Draw a bounding box around every leukocyte (white blood cell).
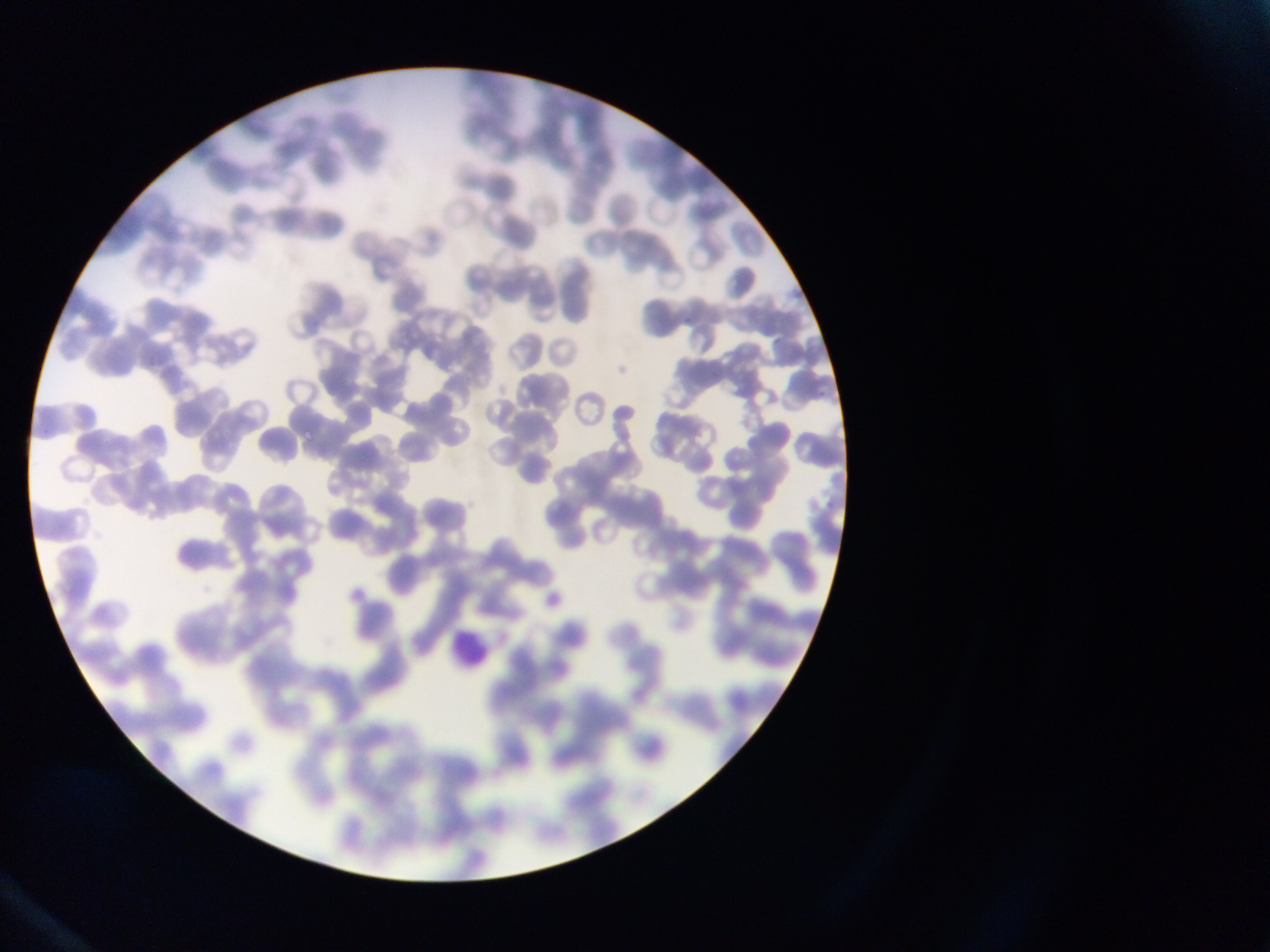

Approximate bounding boxes as {left, top, right, bottom} in pixels.
Leukocytes: {446, 628, 493, 676}.

Summary:
  - Country: Ghana
  - Image size: 1270×952 pixels
  - Preparation: thin blood smear
  - Capture: mobile-phone photograph through a microscope
  - Field of view: single